Name the blood parasite species.
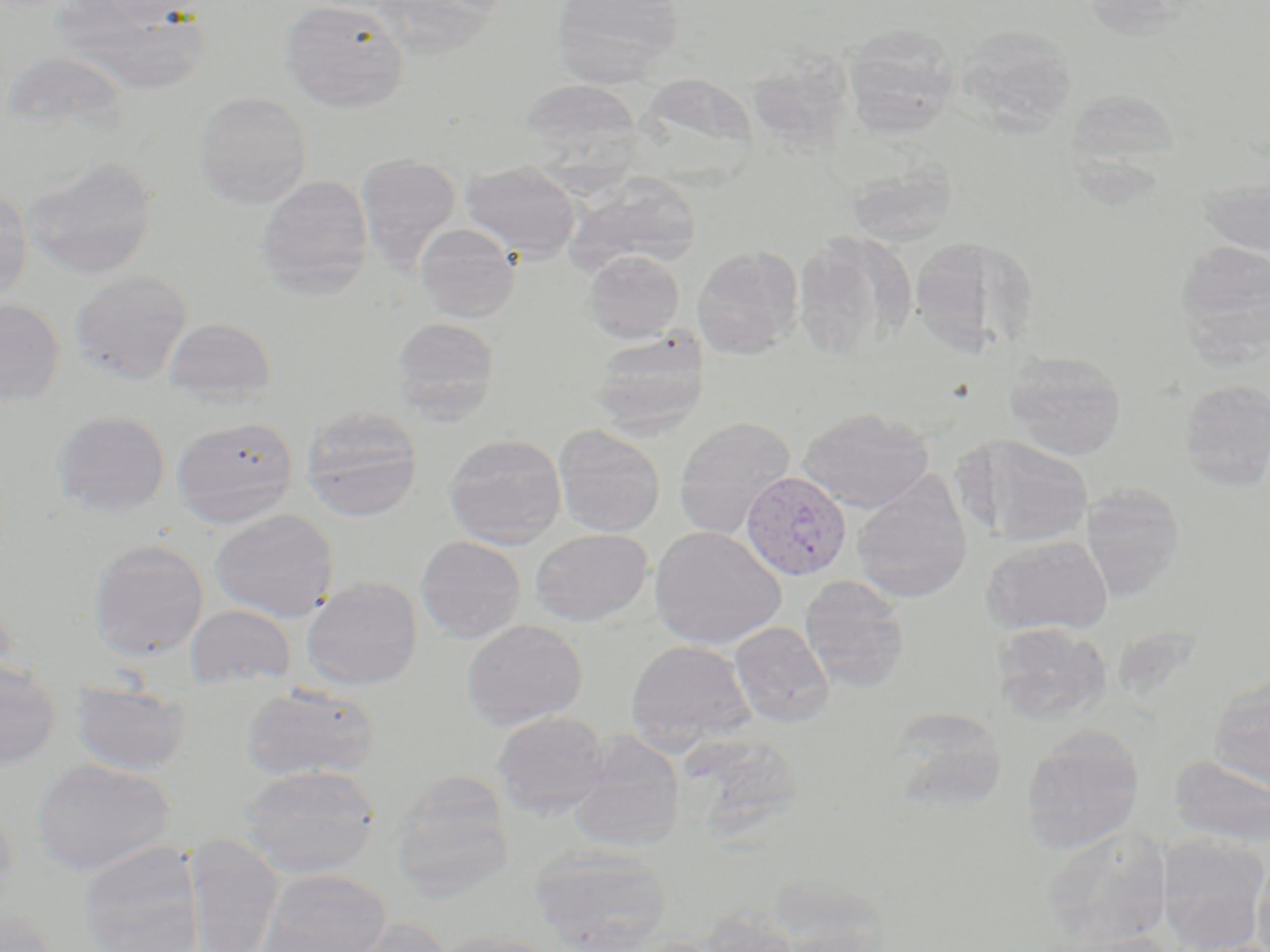
Plasmodium vivax.

Summary:
  - Coordinate format: approximate bounding boxes as (x1,y1)-(x2,y2) corner pairs in pixels
  - Plasmodium vivax-infected red blood cell locations: (740,470)-(854,582)
  - Uninfected red blood cell locations: (53,0)-(209,94), (94,0)-(204,26), (374,0)-(505,58), (550,0)-(685,86), (278,1)-(409,113), (841,24)-(959,139), (956,24)-(1079,132), (753,38)-(864,161), (644,75)-(776,200), (519,79)-(643,168), (1064,88)-(1182,175), (194,92)-(312,208), (356,153)-(461,270), (24,156)-(158,280), (844,156)-(958,248), (462,162)-(580,261), (1199,172)-(1270,262), (256,175)-(374,297), (566,175)-(701,276), (0,187)-(33,305), (415,222)-(521,322), (792,230)-(915,364), (909,236)-(1039,357), (1174,240)-(1270,361), (691,246)-(804,360), (583,250)-(685,343), (69,270)-(193,385), (0,298)-(66,407), (392,317)-(500,422), (163,318)-(277,406), (588,328)-(710,434), (1003,350)-(1127,461), (1179,379)-(1270,490), (299,406)-(424,521), (799,407)-(935,513), (51,410)-(171,518), (171,417)-(300,528), (673,417)-(795,538), (553,425)-(666,537), (443,433)-(567,548), (956,433)-(1096,547), (850,474)-(973,604), (1079,483)-(1185,602), (211,508)-(339,621), (649,525)-(786,649), (530,528)-(653,626), (980,534)-(1114,637), (415,536)-(526,642), (88,539)-(209,661), (302,576)-(422,689), (799,576)-(910,695), (0,594)-(17,694), (185,605)-(297,691), (462,619)-(588,731), (730,621)-(834,728), (990,622)-(1112,725), (625,639)-(757,752), (0,658)-(62,770), (69,679)-(192,774), (1208,679)-(1270,793), (240,684)-(380,783), (887,709)-(1008,814), (492,711)-(611,818), (1020,727)-(1144,855), (570,733)-(686,854), (1170,754)-(1270,847), (30,758)-(176,877), (239,763)-(382,879), (388,774)-(515,901), (0,795)-(18,908), (1039,825)-(1174,948), (184,833)-(284,952), (1157,834)-(1270,951), (78,842)-(204,952), (528,845)-(672,952), (1252,845)-(1270,952), (259,869)-(392,952), (696,907)-(800,952), (0,909)-(63,952), (337,918)-(451,952), (1037,931)-(1174,952), (432,932)-(560,952), (621,936)-(726,952)
  - Stain: May-Grünwald-Giemsa
  - Modality: light microscopy
  - Magnification: 1000x
  - Preparation: thin blood film
  - Field of view: single
  - Image size: 1270×952 pixels